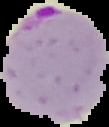

Summary:
  - Preparation: thin blood film
  - Image type: segmented cell region with the area outside set to black
  - Image size: 109×127 pixels
  - Result: Plasmodium parasites identified